Assess this cell for malaria.
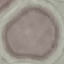
Uninfected.

Giemsa stain. Automatically extracted cell patch, resized to 64 × 64 pixels. Thin smear of blood. Photographed with a smartphone camera at the microscope eyepiece.